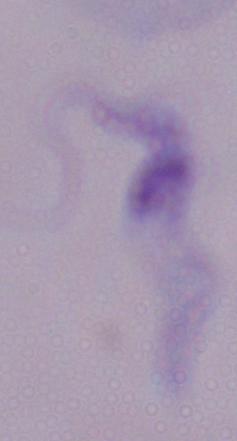

A trypanosome is seen. 1000x magnification. Photomicrograph.